Assess the morphology of the erythrocytes.
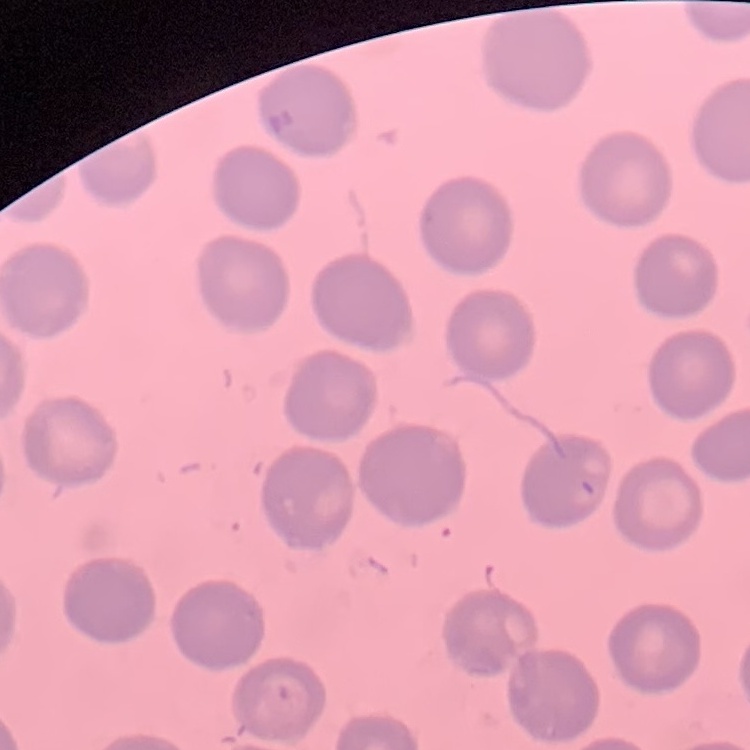

They show no rouleaux formation.

Thin blood film. Square crop of a larger photomicrograph. Field's or Giemsa stain.